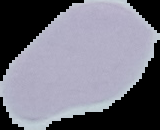

{
  "malaria_status": "uninfected",
  "image_size": "160×130 pixels",
  "image_type": "segmented cell region with the area outside set to black",
  "preparation": "thin blood film"
}